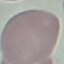
result = negative for malaria parasites
image type = automatically extracted cell patch, resized to 64 × 64 pixels
preparation = thin blood film
stain = Giemsa
capture = smartphone through the microscope eyepiece